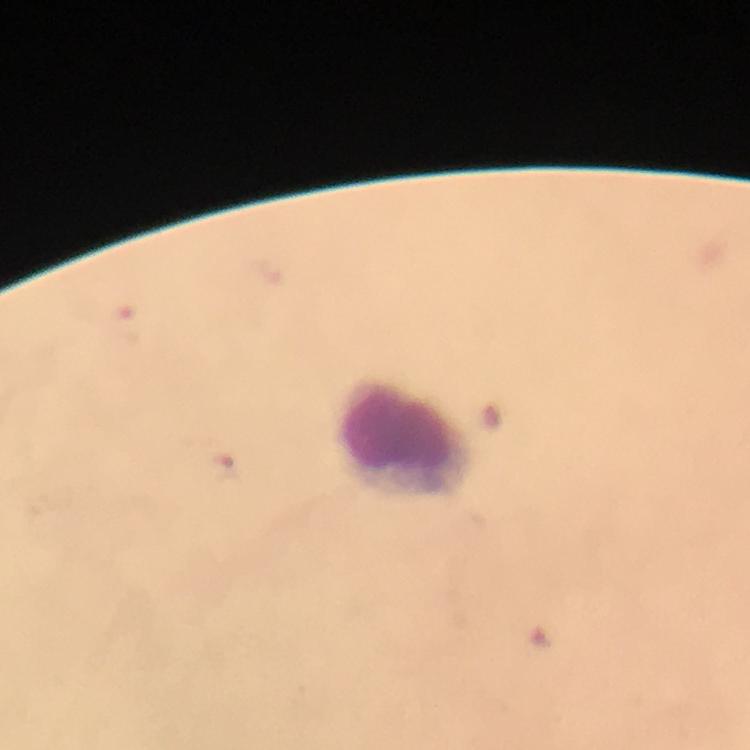

Approximate centers as (x, y) in pixels. Leukocyte locations: (405, 440). 100x magnification. Immersion oil applied. Photographed through the microscope with a smartphone camera. From a malaria diagnostic workup. A crop from one field of view. Image is 750×750 pixels. Plasmodium parasites: none detected. Giemsa-stained preparation. Thick smear.